Locate every Plasmodium parasite.
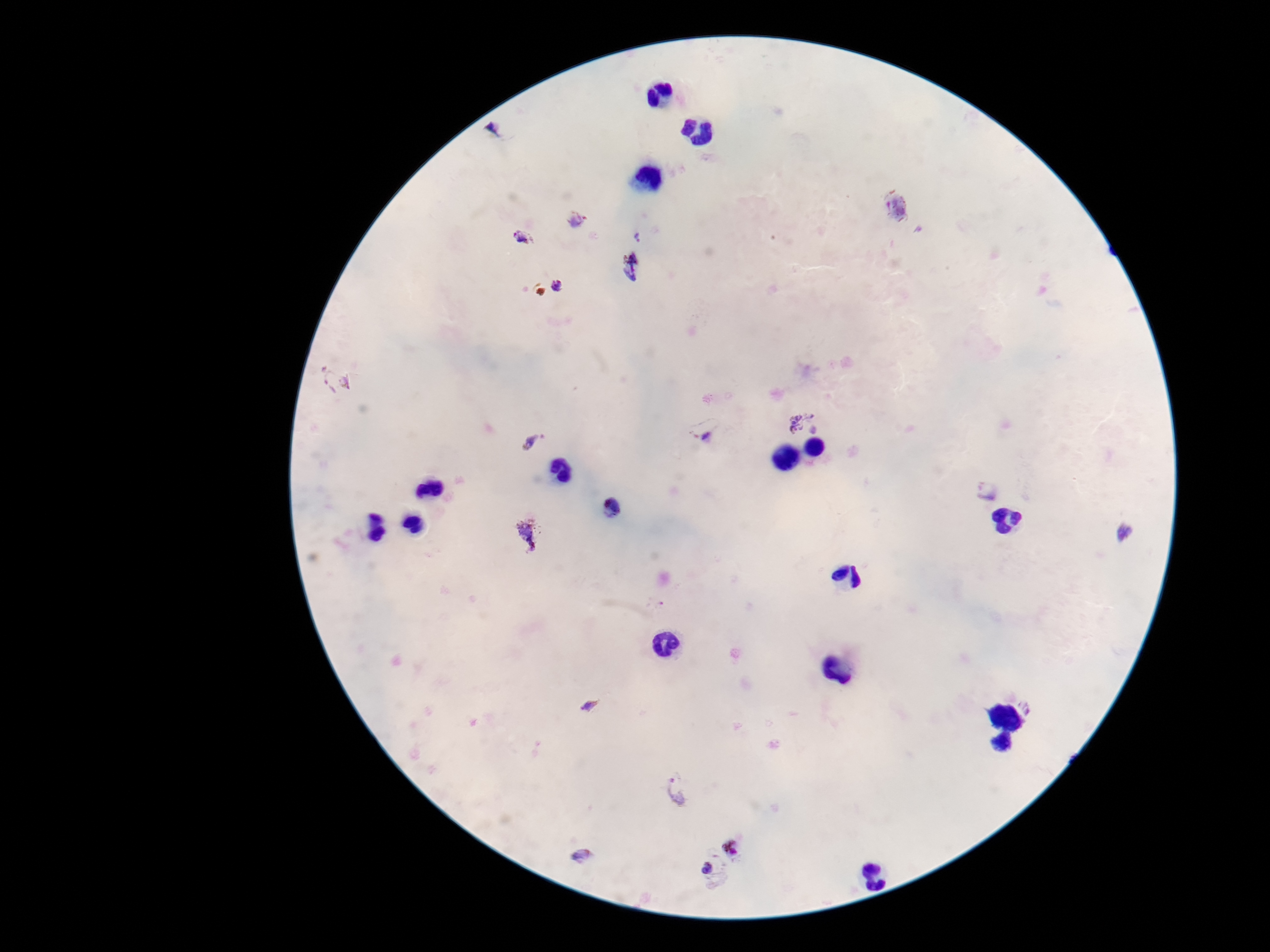

Approximate centers as {x, y} in pixels.
Plasmodium parasites: {494, 129}, {896, 207}, {577, 219}, {639, 236}, {521, 237}, {631, 269}, {558, 288}, {336, 381}, {798, 421}, {705, 429}, {530, 443}, {988, 490}, {529, 531}, {1124, 531}, {589, 705}, {677, 789}, {732, 847}, {582, 855}, {708, 868}.

Summary:
  - Field of view: single
  - Patient malaria status: positive
  - Image size: 1270×952 pixels
  - Preparation: thick blood film
  - Capture: smartphone camera through the microscope eyepiece
  - Stain: Giemsa
  - Magnification: 100x